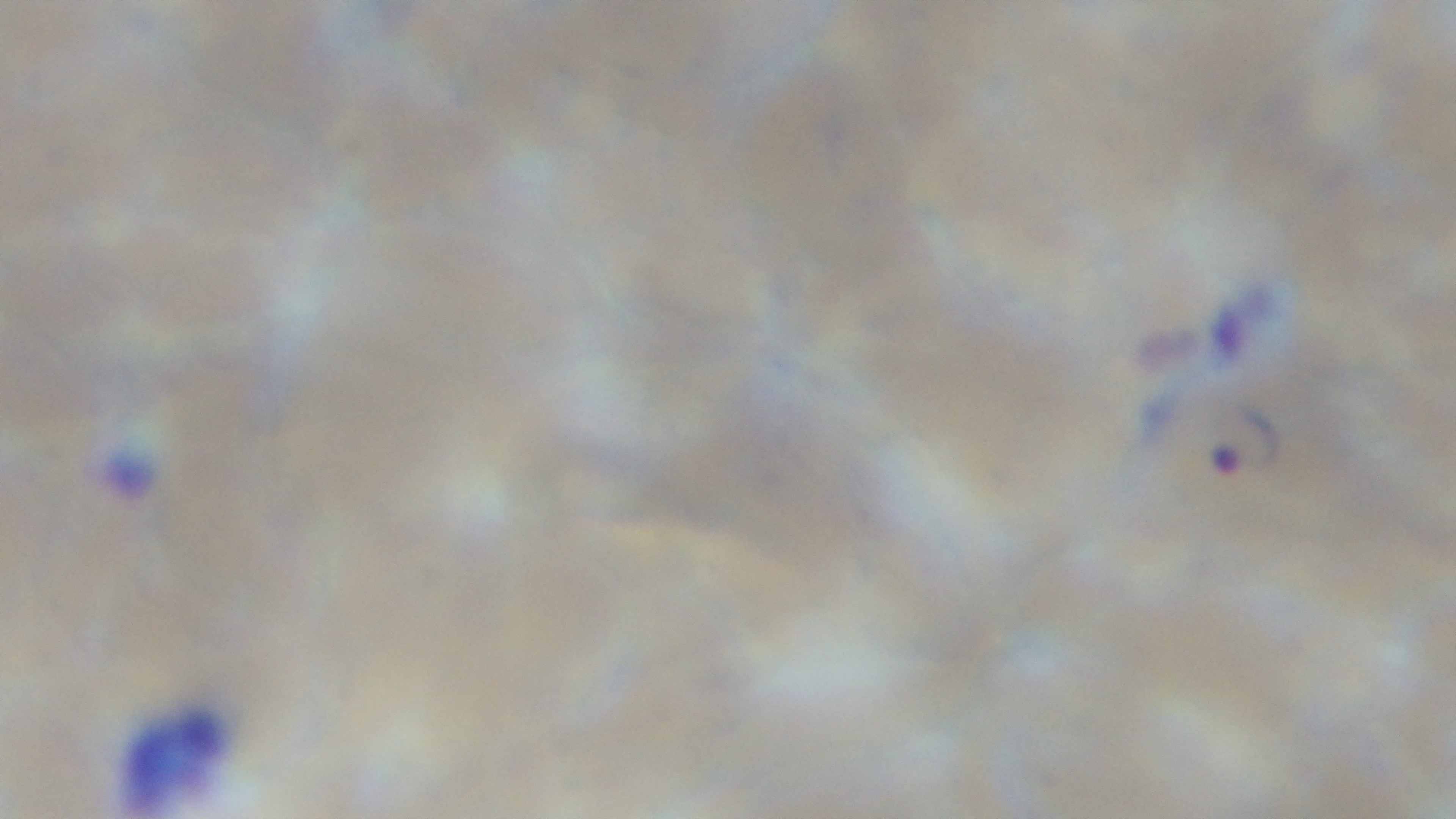

Summary:
  - Preparation: thin smear
  - Capture: mounted 4K digital camera
  - Malaria status: positive
  - Modality: light microscopy
  - Field of view: single
  - Objective: 100x oil immersion
  - Stain: Giemsa